Outline platelets.
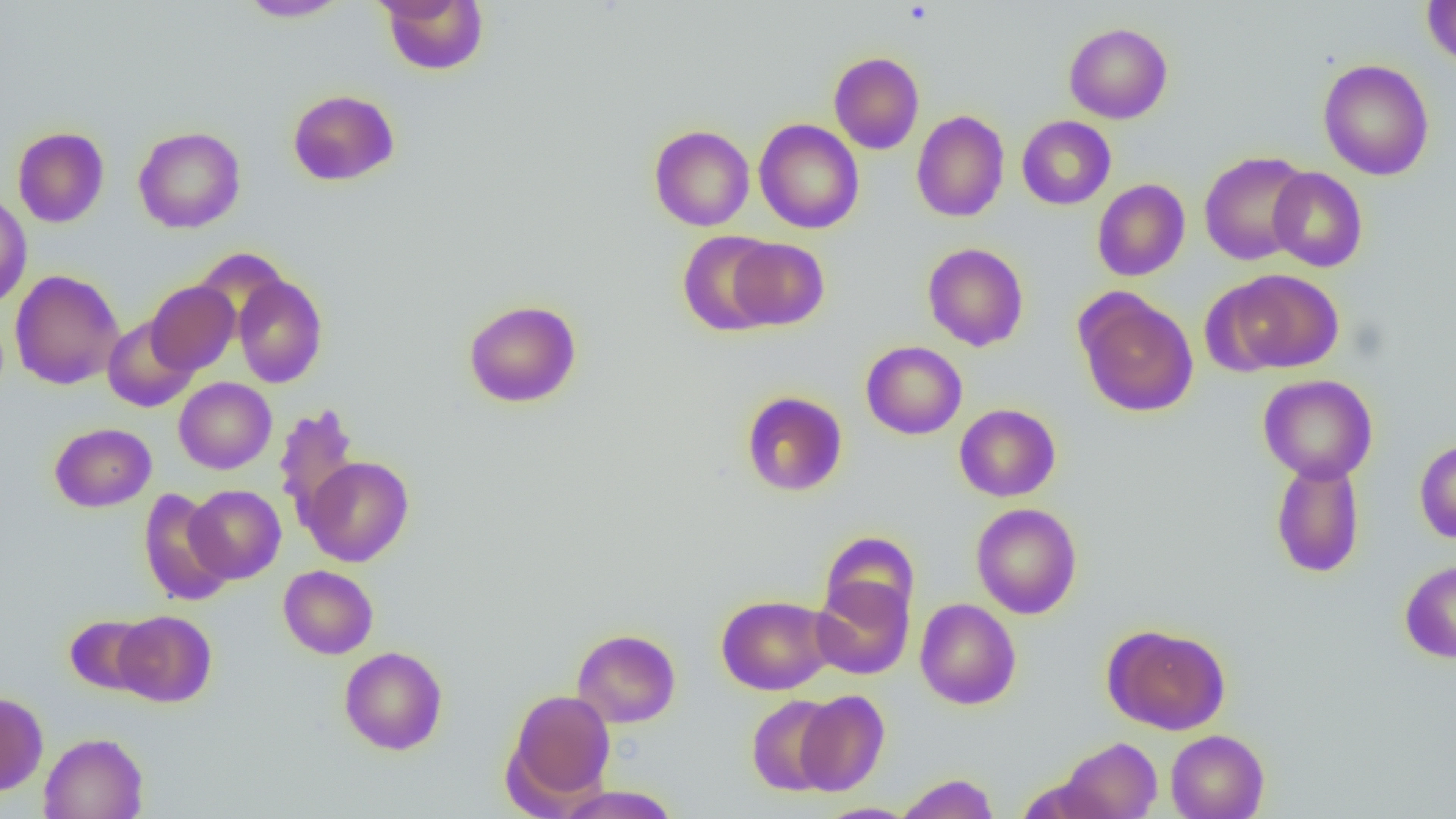
Approximate bounding boxes as (x1,y1)-(x2,y2) corner pairs in pixels.
Platelets: (902,2)-(933,26).

{
  "slide_level_diagnosis": "negative for blood parasites",
  "image_size": "1456×819 pixels",
  "modality": "light microscopy",
  "preparation": "thin blood smear",
  "field_of_view": "one of a larger specimen",
  "magnification": "1000x",
  "uninfected_red_blood_cell_locations": "approximate bounding boxes as (x1,y1)-(x2,y2) corner pairs in pixels: (238,0)-(352,22), (378,0)-(489,75), (1422,1)-(1456,69), (1064,22)-(1173,123), (828,52)-(924,154), (1317,59)-(1434,180), (287,89)-(399,186), (911,110)-(1009,222), (1017,115)-(1116,209), (754,118)-(864,234), (649,124)-(755,231), (12,126)-(109,228), (133,127)-(246,233), (1199,152)-(1312,265), (1267,167)-(1367,272), (1092,179)-(1190,281), (0,193)-(32,309), (677,231)-(780,337), (728,238)-(829,329), (923,243)-(1029,351), (1217,268)-(1343,374), (10,269)-(125,389), (233,274)-(328,388), (146,281)-(240,374), (1076,290)-(1198,418), (463,299)-(582,408), (102,315)-(199,412), (861,341)-(967,439), (1258,374)-(1378,483), (174,377)-(276,474), (741,391)-(847,496), (954,403)-(1061,502), (273,404)-(361,529), (49,422)-(156,512), (1414,439)-(1456,543), (302,456)-(414,566), (1271,457)-(1365,578), (186,485)-(286,584), (138,489)-(234,606), (971,503)-(1082,619), (820,530)-(919,626), (1399,560)-(1456,662), (278,565)-(378,659), (810,576)-(915,680), (716,595)-(834,695), (914,598)-(1021,710), (113,610)-(217,707), (64,614)-(158,696), (1103,624)-(1231,735), (572,629)-(681,728), (339,646)-(448,755), (505,689)-(616,806), (795,689)-(890,797), (0,692)-(49,795), (747,694)-(841,796), (1166,729)-(1269,819), (39,732)-(148,819), (1056,737)-(1162,819), (895,773)-(999,819), (554,785)-(681,818), (816,803)-(920,819)"
}